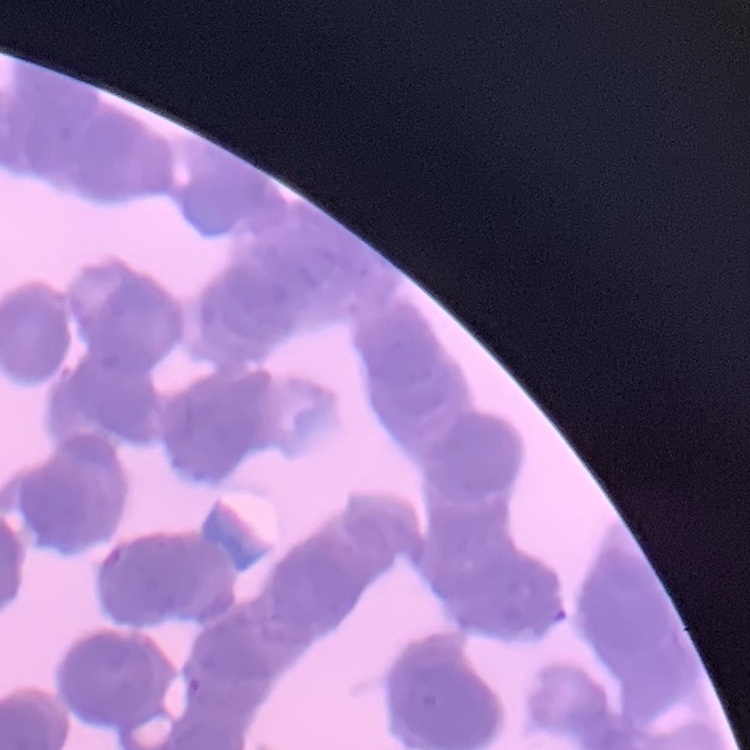
erythrocyte_morphology: rouleaux formation
image_type: square crop of a larger photomicrograph
preparation: thin peripheral smear
stain: Field's or Giemsa